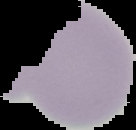
{
  "preparation": "thin blood smear",
  "malaria_status": "uninfected",
  "image_type": "cell region segmented out of the field of view; surrounding area masked to black",
  "image_size": "136×130 pixels"
}